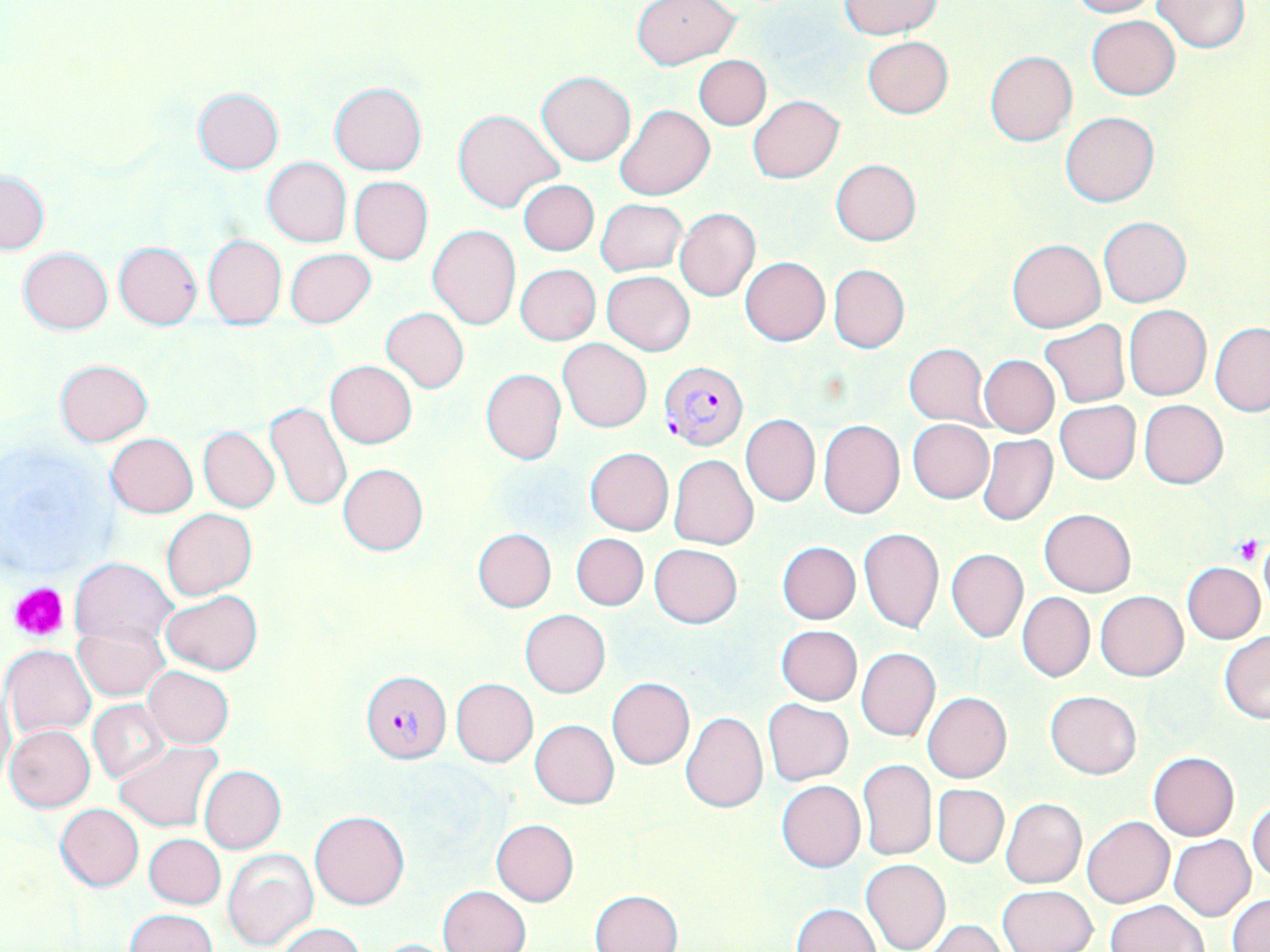
Approximate bounding boxes as (x1,y1)-(x2,y2) corner pairs in pixels. Plasmodium falciparum-infected red blood cell locations: (659,361)-(748,450), (361,670)-(451,763). Uninfected red blood cell locations: (631,0)-(741,70), (1066,0)-(1159,18), (840,1)-(941,38), (1152,1)-(1249,53), (1086,15)-(1180,100), (863,36)-(953,118), (985,50)-(1078,145), (694,55)-(771,130), (536,70)-(636,166), (329,82)-(427,175), (193,87)-(284,173), (748,95)-(844,183), (614,104)-(714,201), (452,110)-(563,213), (1062,112)-(1161,206), (262,158)-(351,248), (830,159)-(921,245), (1,171)-(49,254), (350,177)-(433,264), (518,180)-(599,255), (595,198)-(687,276), (675,208)-(760,301), (1098,215)-(1192,308), (426,224)-(521,330), (202,235)-(287,329), (1006,238)-(1107,332), (114,242)-(203,328), (19,247)-(113,334), (286,248)-(374,328), (739,257)-(830,346), (828,263)-(909,353), (515,264)-(601,345), (601,271)-(694,355), (1124,305)-(1210,400), (379,307)-(470,393), (1040,319)-(1130,408), (1210,324)-(1270,415), (558,339)-(652,432), (904,343)-(990,427), (980,355)-(1059,437), (55,358)-(152,445), (325,360)-(417,448), (480,367)-(566,464), (1139,400)-(1228,489), (1055,401)-(1140,483), (265,402)-(352,512), (741,414)-(820,507), (818,420)-(905,519), (908,420)-(993,503), (198,427)-(280,512), (105,433)-(199,517), (976,433)-(1057,526), (584,447)-(674,536), (668,455)-(759,550), (338,463)-(428,556), (163,508)-(256,599), (1038,509)-(1136,596), (858,527)-(944,633), (473,528)-(556,612), (571,533)-(647,610), (777,541)-(860,624), (650,545)-(741,628), (947,549)-(1028,642), (70,557)-(176,646), (1183,562)-(1266,643), (160,590)-(262,674), (1095,590)-(1189,681), (1018,592)-(1094,681), (520,610)-(610,698), (74,625)-(166,700), (775,626)-(863,705), (1219,631)-(1270,723), (3,644)-(96,738), (856,648)-(940,741), (143,667)-(234,749), (607,677)-(696,770), (451,678)-(538,767), (1,686)-(15,790), (1045,690)-(1141,779), (923,692)-(1012,783), (88,699)-(171,784), (763,699)-(854,786), (680,712)-(768,814), (530,720)-(619,809), (4,724)-(96,812), (113,741)-(222,832), (1149,751)-(1239,841), (858,759)-(936,861), (199,765)-(285,853), (776,780)-(866,873), (933,784)-(1008,867), (1001,798)-(1086,888), (1248,800)-(1270,884), (56,804)-(144,891), (310,810)-(409,910), (1082,815)-(1175,907), (491,819)-(578,905), (145,834)-(225,908), (1169,835)-(1255,920), (223,850)-(318,951), (861,858)-(950,952), (437,885)-(531,952), (997,885)-(1096,952), (591,889)-(684,952), (1228,893)-(1270,952), (1103,900)-(1207,951), (789,903)-(881,951), (125,908)-(217,952), (924,920)-(1006,952), (276,923)-(364,952), (368,938)-(466,951). Platelet locations: (1235,537)-(1263,564), (9,582)-(70,642). Slide-level diagnosis: Plasmodium falciparum. Image is 1270×952 pixels. Single field of view. Light microscopy. May-Grünwald-Giemsa-stained preparation. Thin blood film. 1000x magnification.